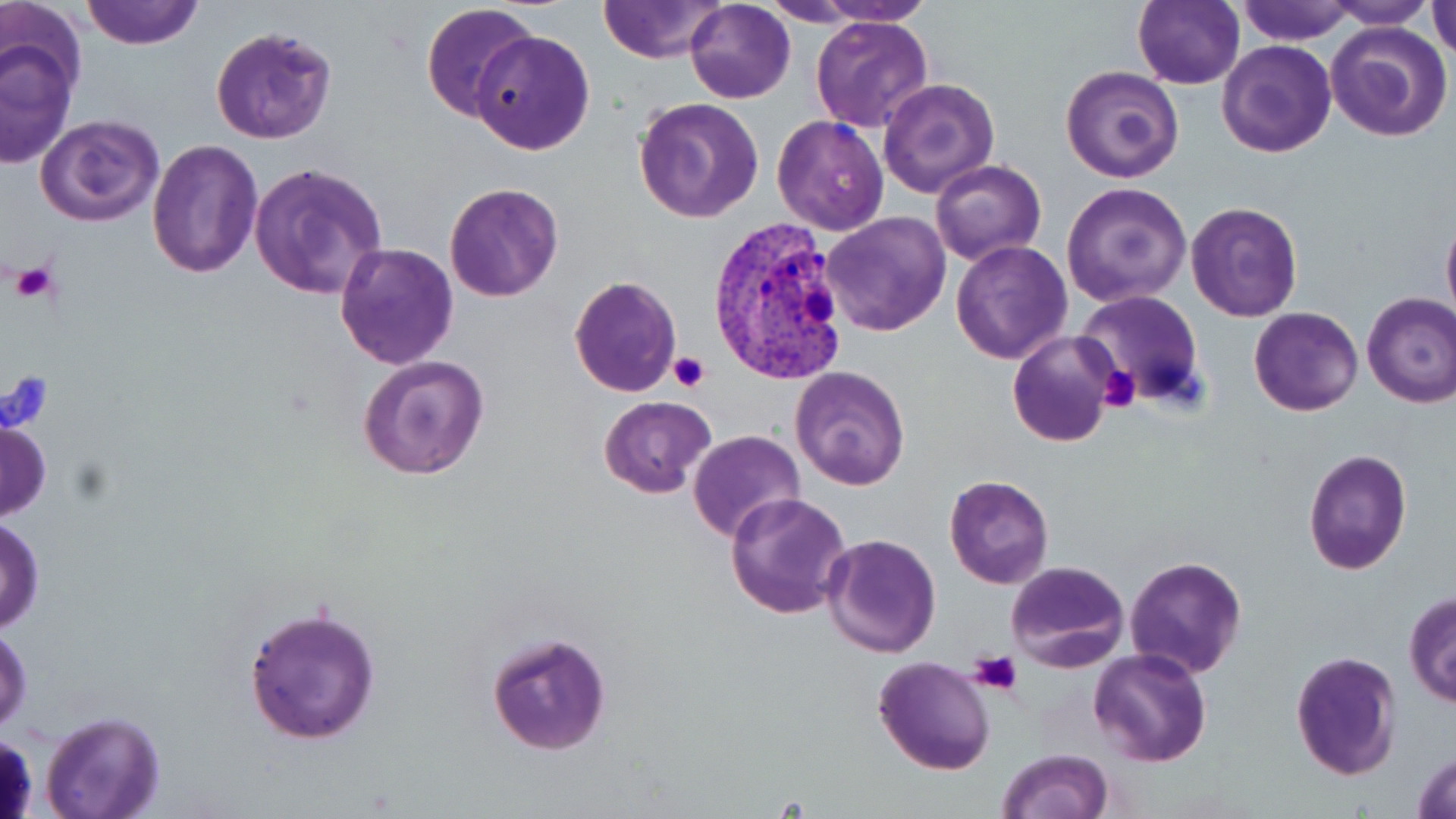

{
  "slide_level_diagnosis": "Plasmodium vivax",
  "stain": "May-Grünwald-Giemsa",
  "uninfected_red_blood_cell_locations": "approximate bounding boxes as (x1, y1, x2, y2) in pixels: (81, 0, 202, 49), (597, 0, 730, 65), (798, 0, 939, 27), (1133, 0, 1243, 89), (1233, 0, 1358, 44), (1321, 0, 1438, 28), (684, 1, 795, 102), (0, 2, 87, 96), (420, 3, 539, 124), (1427, 3, 1456, 58), (808, 13, 934, 133), (1325, 20, 1453, 142), (210, 25, 335, 144), (471, 28, 594, 154), (0, 38, 77, 170), (1217, 39, 1337, 157), (1059, 65, 1185, 184), (877, 79, 1001, 199), (634, 98, 765, 223), (34, 113, 165, 226), (771, 115, 890, 237), (145, 140, 265, 279), (930, 160, 1046, 267), (248, 163, 389, 302), (444, 181, 564, 302), (1061, 182, 1192, 306), (1186, 201, 1304, 321), (820, 212, 951, 337), (1441, 212, 1456, 328), (951, 240, 1073, 364), (333, 241, 458, 370), (569, 275, 682, 396), (1073, 290, 1205, 411), (1361, 292, 1456, 408), (1249, 305, 1362, 417), (1007, 330, 1116, 447), (358, 355, 489, 480), (789, 366, 910, 490), (599, 395, 716, 498), (0, 419, 51, 520), (688, 429, 806, 542), (1303, 450, 1411, 574), (943, 475, 1054, 589), (726, 491, 853, 619), (0, 517, 45, 632), (821, 534, 943, 659), (1124, 554, 1249, 680), (1005, 559, 1130, 672), (1403, 591, 1456, 708), (242, 604, 383, 744), (1, 624, 32, 735), (484, 629, 612, 756), (1089, 648, 1215, 767), (1289, 650, 1403, 780), (873, 655, 996, 775), (40, 711, 164, 819), (996, 749, 1113, 819), (1412, 750, 1456, 819)",
  "magnification": "1000x",
  "image_size": "1456×819 pixels",
  "modality": "optical microscopy",
  "field_of_view": "single",
  "preparation": "thin blood film",
  "plasmodium_vivax_infected_red_blood_cell_locations": "approximate bounding boxes as (x1, y1, x2, y2) in pixels: (709, 215, 852, 385)",
  "platelet_locations": "approximate bounding boxes as (x1, y1, x2, y2) in pixels: (9, 260, 57, 307), (668, 350, 709, 392), (1097, 365, 1143, 411), (0, 373, 53, 433), (970, 651, 1022, 698)"
}